Identify the parasite.
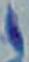

This is Toxoplasma gondii.

modality = photomicrograph
magnification = 1000x